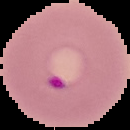

Result: malaria parasites detected. From a thin blood smear. Image is 130×130 pixels. The area outside the segmented cell region is set to black.